Locate every malaria parasite by life-cycle stage, and every leukocyte.
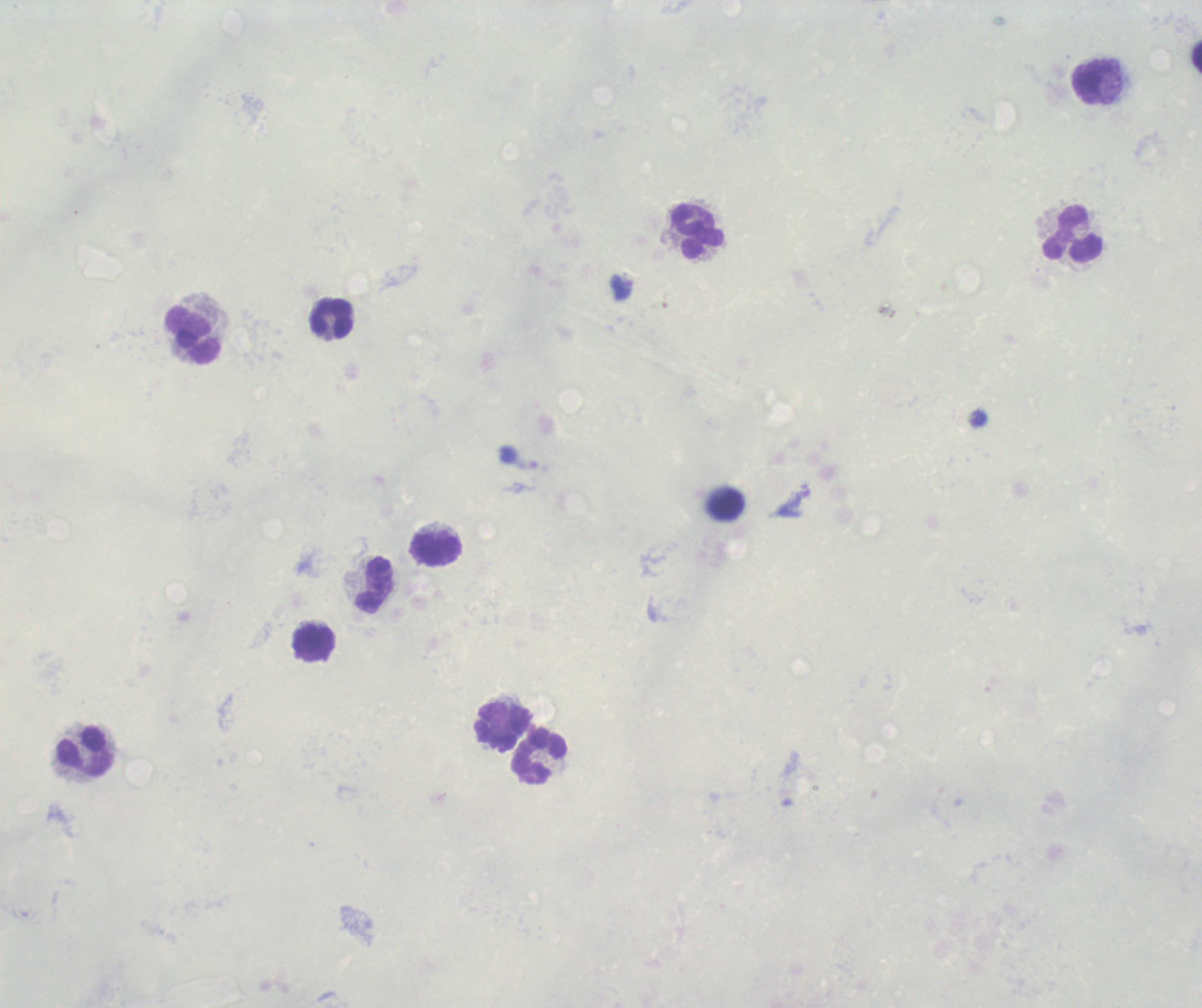
Approximate object centers, in pixels from the top-left corner.
Trophozoites: (x=622, y=287).
No schizont or gametocyte forms observed.
Leukocytes: (x=1092, y=83), (x=698, y=231), (x=1073, y=234), (x=332, y=319), (x=193, y=335), (x=438, y=549), (x=375, y=586), (x=314, y=644), (x=504, y=726), (x=85, y=753), (x=539, y=758).

Summary:
  - Field of view: single
  - Magnification: 100x
  - Background quality: poor
  - Context: previously used in an actual diagnosis
  - Preparation: thick blood smear
  - Image size: 1202×1008 pixels
  - Stain: Romanowsky